Report the malaria status of this cell.
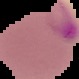

It is parasitized.

image size = 79×79 pixels
image type = segmented cell region with the area outside set to black
preparation = thin blood film